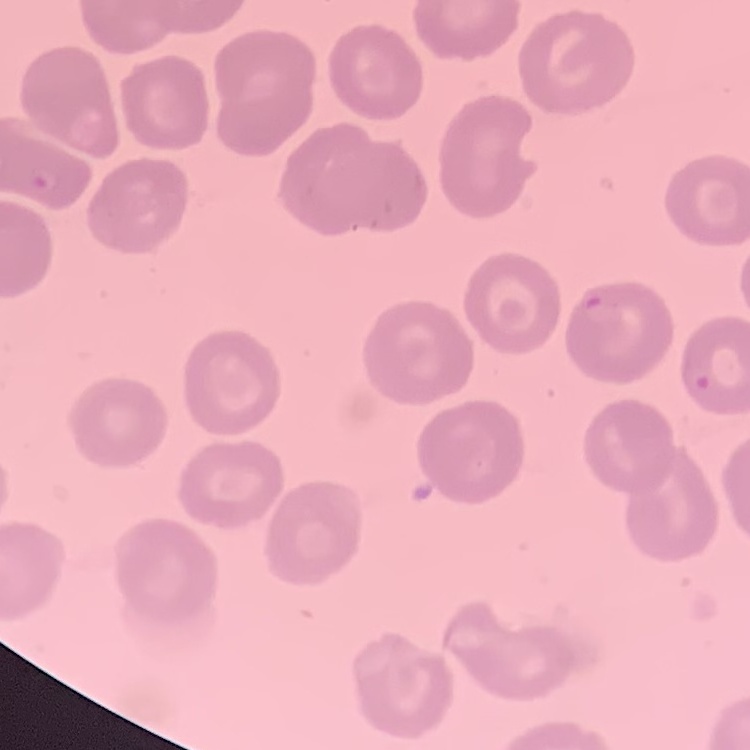 The erythrocytes show no rouleaux formation. Stained with either Field's or Giemsa. Thin blood film. One tile cut from a larger photomicrograph.